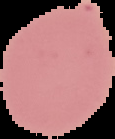
image_type: segmented cell region on a black background
image_size: 115×139 pixels
preparation: thin blood film
malaria_status: uninfected